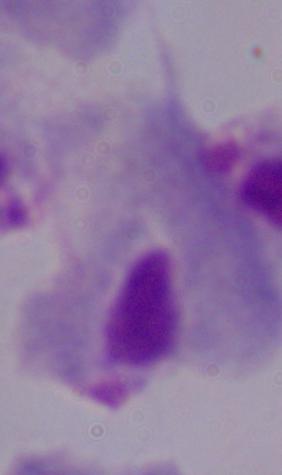

A trichomonad is shown. Captured at 1000x magnification. Photomicrograph.